Report the malaria status of this cell.
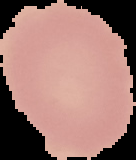

It is uninfected.

preparation = thin blood smear
image size = 136×160 pixels
image type = cell region segmented out of the field of view; surrounding area masked to black